State the blood parasite species.
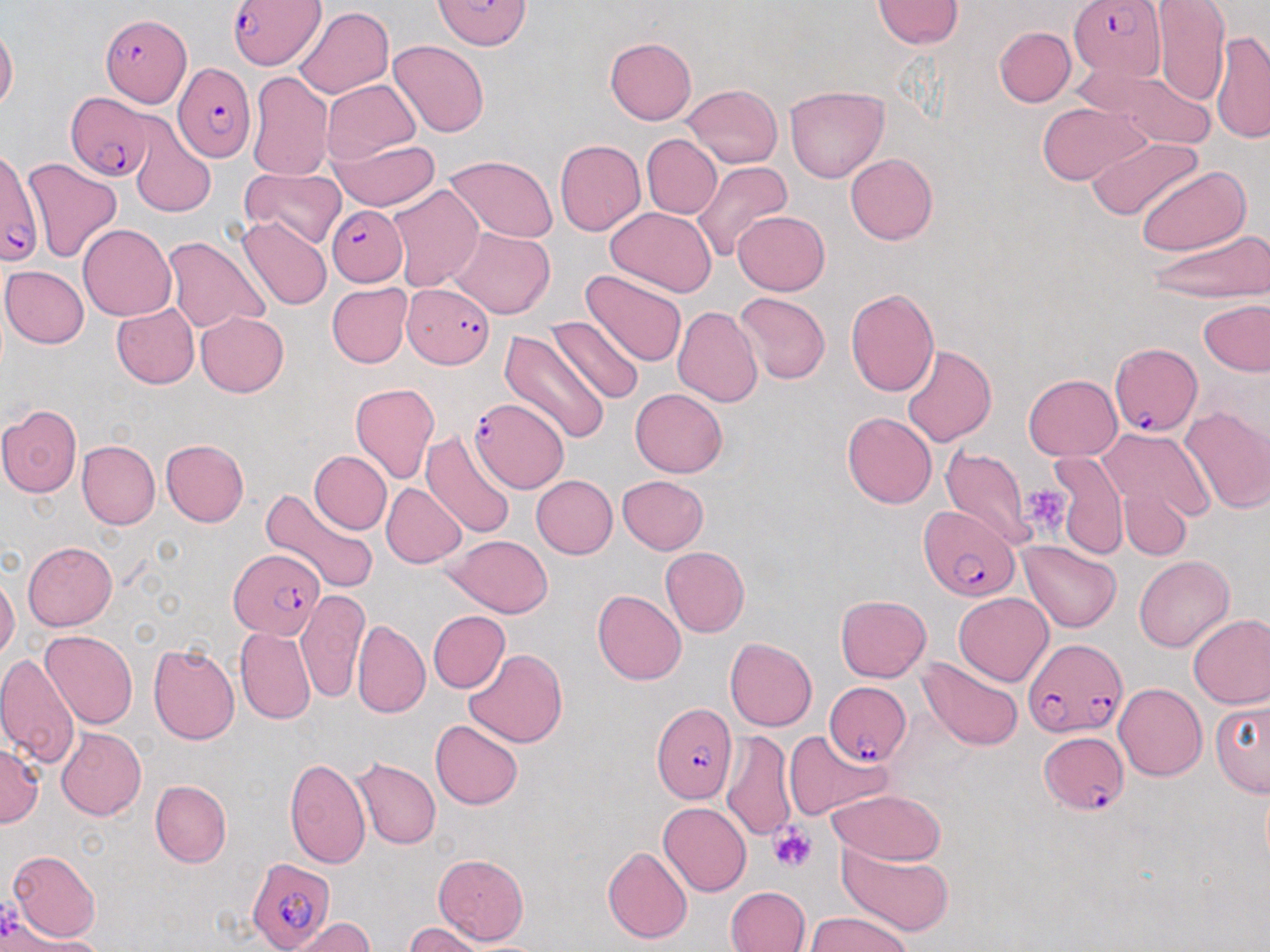

Plasmodium falciparum.

uninfected red blood cell locations = approximate bounding boxes as (x1,y1)-(x2,y2) corner pairs in pixels: (1150,0)-(1230,104), (872,1)-(963,49), (294,7)-(394,99), (0,25)-(18,111), (994,26)-(1075,107), (1209,30)-(1270,146), (605,37)-(697,124), (389,40)-(488,137), (1072,63)-(1215,150), (247,70)-(334,182), (323,79)-(420,165), (682,84)-(783,168), (784,84)-(888,183), (1037,102)-(1149,185), (130,126)-(215,217), (643,135)-(722,218), (1088,136)-(1203,222), (329,137)-(440,212), (554,140)-(645,235), (845,153)-(938,245), (443,155)-(559,244), (21,157)-(123,265), (690,161)-(792,263), (1136,164)-(1250,255), (239,166)-(346,249), (387,183)-(484,292), (604,206)-(717,296), (733,210)-(830,295), (238,217)-(332,311), (77,224)-(175,321), (450,228)-(555,319), (1147,228)-(1269,303), (164,237)-(270,335), (1,265)-(89,348), (582,270)-(687,368), (327,282)-(413,367), (846,287)-(940,397), (732,293)-(832,385), (1198,298)-(1270,377), (110,302)-(199,389), (672,305)-(764,406), (196,312)-(289,397), (549,315)-(644,405), (498,329)-(610,444), (902,344)-(996,446), (1025,374)-(1122,460), (349,382)-(439,484), (631,388)-(728,477), (383,398)-(499,516), (0,404)-(83,497), (1178,405)-(1270,514), (842,412)-(937,508), (1100,427)-(1215,522), (422,429)-(517,537), (76,439)-(160,529), (161,439)-(248,527), (941,446)-(1035,547), (1052,449)-(1129,559), (310,451)-(391,534), (531,475)-(618,559), (617,475)-(709,555), (381,483)-(466,568), (1117,483)-(1194,562), (259,487)-(378,595), (446,534)-(553,617), (1019,540)-(1121,633), (21,541)-(116,631), (659,547)-(749,637), (1134,555)-(1234,652), (0,573)-(20,661), (592,588)-(686,685), (297,590)-(367,703), (954,592)-(1053,686), (835,595)-(931,682), (428,610)-(510,693), (1187,613)-(1270,709), (352,619)-(430,717), (235,627)-(315,724), (41,630)-(138,729), (725,637)-(817,731), (148,643)-(240,744), (463,649)-(568,749), (0,652)-(82,768), (916,656)-(1024,751), (1114,683)-(1207,781), (1209,697)-(1269,798), (430,719)-(522,809), (56,727)-(146,820), (784,729)-(891,822), (721,730)-(797,843), (0,744)-(43,828), (349,757)-(441,850), (284,758)-(371,869), (150,779)-(232,867), (827,788)-(947,865), (658,802)-(751,896), (602,846)-(692,943), (839,846)-(953,935), (8,850)-(100,942), (433,854)-(529,945), (725,886)-(809,952), (806,911)-(912,952), (284,917)-(373,952), (404,922)-(490,952)
magnification = 1000x
platelet locations = approximate bounding boxes as (x1,y1)-(x2,y2) corner pairs in pixels: (1023,485)-(1072,536), (769,826)-(815,873)
preparation = thin blood smear
field of view = one of a larger specimen
image size = 1270×952 pixels
stain = May-Grünwald-Giemsa
Plasmodium falciparum-infected red blood cell locations = approximate bounding boxes as (x1,y1)-(x2,y2) corner pairs in pixels: (229,0)-(325,71), (432,0)-(533,50), (1069,0)-(1166,83), (102,14)-(188,106), (172,63)-(254,163), (66,92)-(155,181), (1,147)-(43,266), (326,204)-(407,285), (403,281)-(496,368), (1108,341)-(1201,435), (469,398)-(568,491), (920,503)-(1020,604), (231,546)-(328,640), (1023,637)-(1124,737), (824,681)-(911,767), (652,703)-(738,803), (1038,730)-(1130,817), (245,858)-(337,952)
modality = optical microscopy